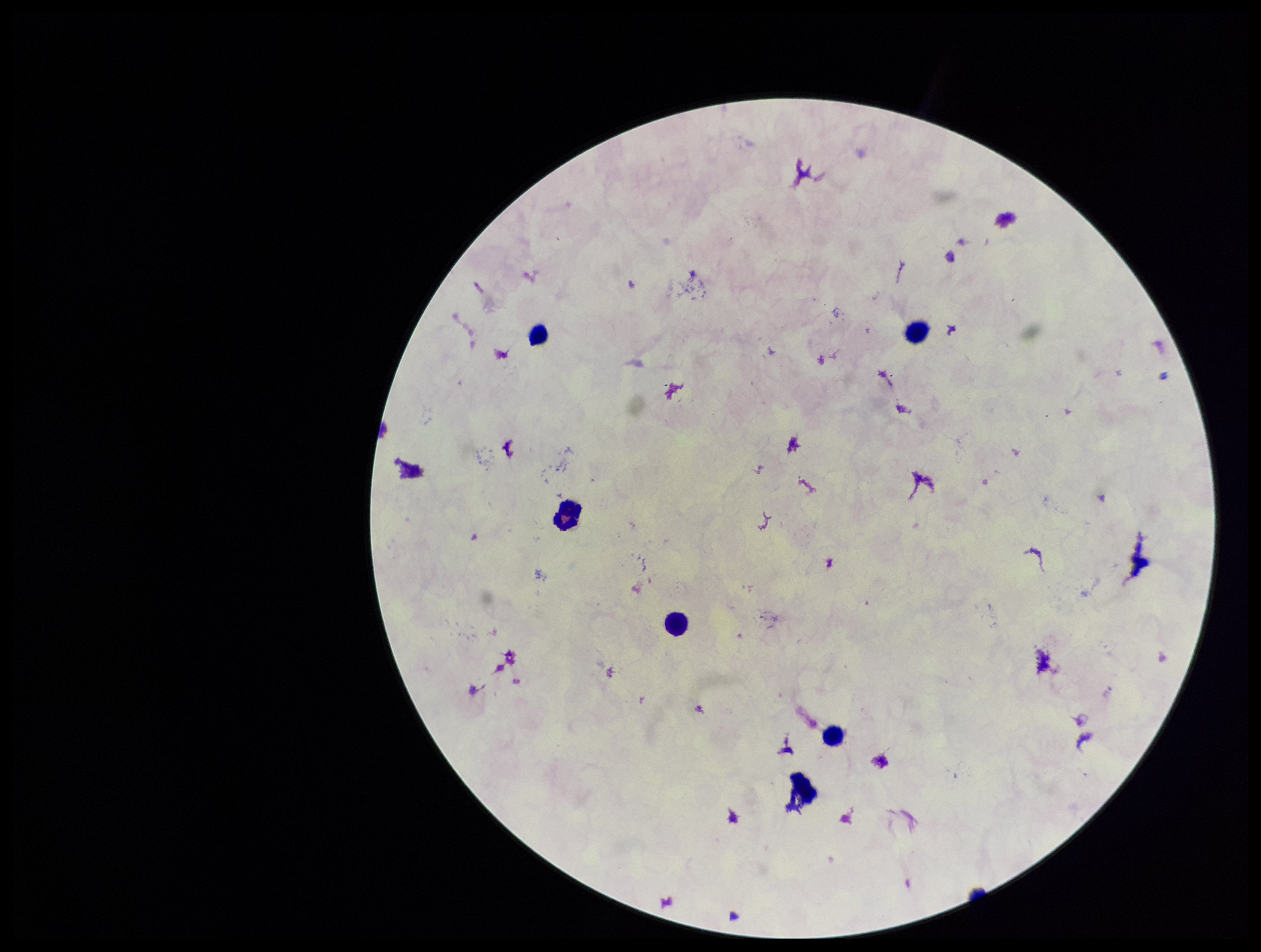
Plasmodium parasites: none seen. Leukocyte count: 6. Patient malaria status: negative. Parasite count: 0. Giemsa stain. Image is 1261×952 pixels. Smartphone photograph taken through the eyepiece of a microscope. Preparation: thick. One field from this slide.